Report the malaria status of this cell.
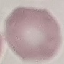

Uninfected.

Summary:
  - Image type: cell patch, automatically extracted from a larger field of view and resized to 64 × 64 pixels
  - Capture: smartphone camera at the microscope eyepiece
  - Preparation: thin smear
  - Stain: Giemsa